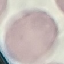

Summary:
  - Result: negative for malaria parasites
  - Preparation: thin blood film
  - Image type: cell patch, automatically extracted from a larger field of view and resized to 64 × 64 pixels
  - Stain: Giemsa
  - Capture: smartphone through the microscope eyepiece